Report the malaria status of this cell.
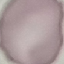

It is uninfected.

capture = smartphone camera at the microscope eyepiece
image type = automatically extracted cell patch, resized to 64 × 64 pixels
stain = Giemsa
preparation = thin blood smear